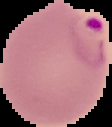

Summary:
  - Malaria status: parasitized
  - Preparation: thin blood film
  - Image size: 112×127 pixels
  - Image type: segmented cell region with the area outside set to black